Locate every Plasmodium parasite.
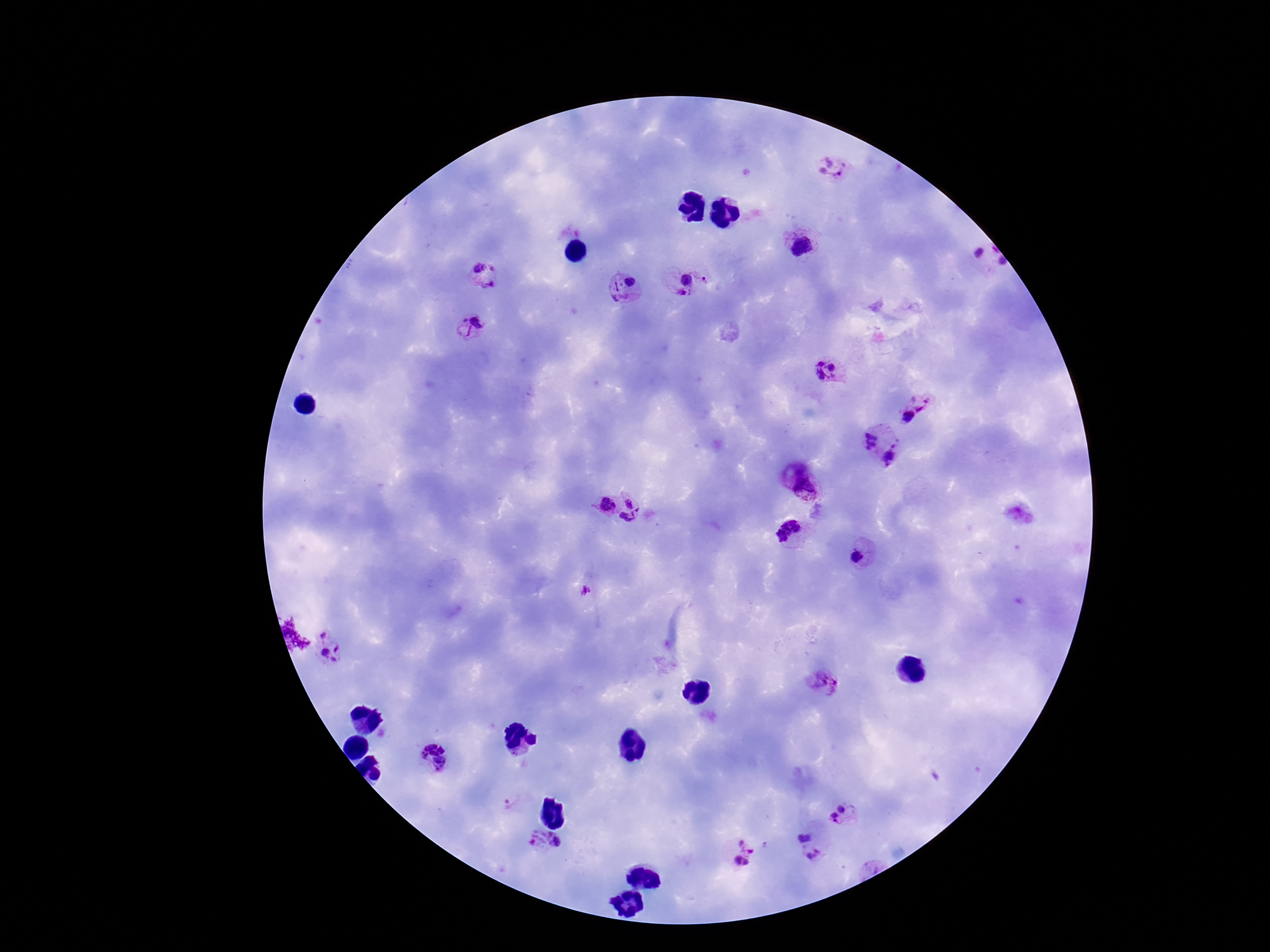

Approximate centers as [x, y] in pixels.
Plasmodium parasites: [836, 166], [801, 248], [982, 263], [487, 277], [684, 279], [625, 290], [470, 325], [827, 372], [916, 408], [867, 439], [894, 456], [807, 488], [604, 505], [634, 511], [791, 532], [858, 552], [333, 645], [820, 681], [432, 757], [510, 805], [845, 805], [836, 817], [804, 836], [544, 842], [743, 854], [815, 856].

Summary:
  - Field of view: single
  - Magnification: 100x
  - Image size: 1270×952 pixels
  - Patient malaria status: positive
  - Preparation: thick peripheral-blood smear
  - Stain: Giemsa
  - Capture: smartphone camera through the microscope eyepiece